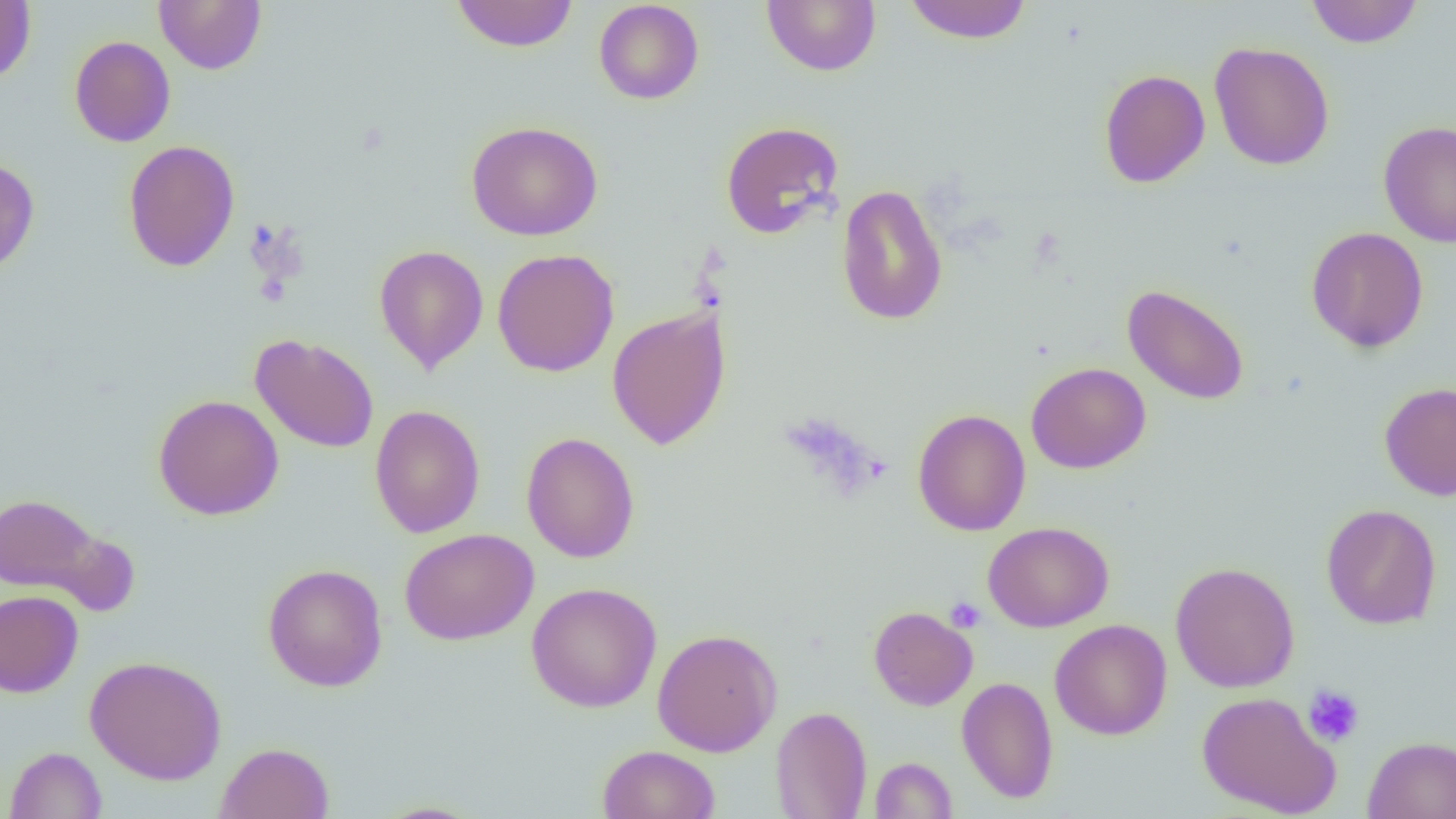
slide-level diagnosis = negative for blood parasites
image size = 1456×819 pixels
magnification = 1000x
uninfected red blood cell locations = approximate bounding boxes as (x1, y1, x2, y2) in pixels: (155, 0, 267, 75), (450, 0, 579, 53), (593, 0, 704, 104), (762, 0, 881, 76), (902, 0, 1033, 44), (1305, 0, 1422, 48), (0, 1, 36, 85), (69, 35, 175, 147), (1209, 41, 1335, 170), (1099, 69, 1211, 188), (465, 121, 603, 241), (720, 121, 844, 240), (1378, 121, 1456, 249), (122, 140, 240, 272), (0, 158, 39, 279), (836, 184, 948, 326), (1306, 226, 1428, 353), (373, 244, 489, 374), (492, 248, 620, 377), (1122, 284, 1250, 405), (607, 306, 731, 450), (249, 333, 379, 453), (1026, 362, 1151, 474), (1379, 382, 1456, 500), (153, 394, 284, 520), (370, 405, 485, 538), (913, 408, 1031, 537), (521, 432, 640, 563), (0, 492, 111, 599), (1321, 504, 1441, 629), (983, 521, 1114, 632), (399, 528, 539, 645), (1170, 561, 1300, 692), (262, 563, 388, 691), (526, 581, 662, 713), (0, 590, 83, 697), (868, 606, 978, 710), (1049, 619, 1172, 740), (652, 627, 782, 757), (85, 655, 227, 785), (956, 676, 1058, 804), (1196, 690, 1340, 817), (771, 706, 872, 819), (1363, 735, 1456, 818), (216, 742, 335, 819), (597, 744, 721, 819), (4, 746, 108, 818), (870, 757, 957, 818), (371, 801, 487, 818)
preparation = thin blood film
platelet locations = approximate bounding boxes as (x1, y1, x2, y2) in pixels: (945, 597, 985, 633), (1302, 685, 1365, 747)
field of view = one of a larger specimen
modality = optical microscopy